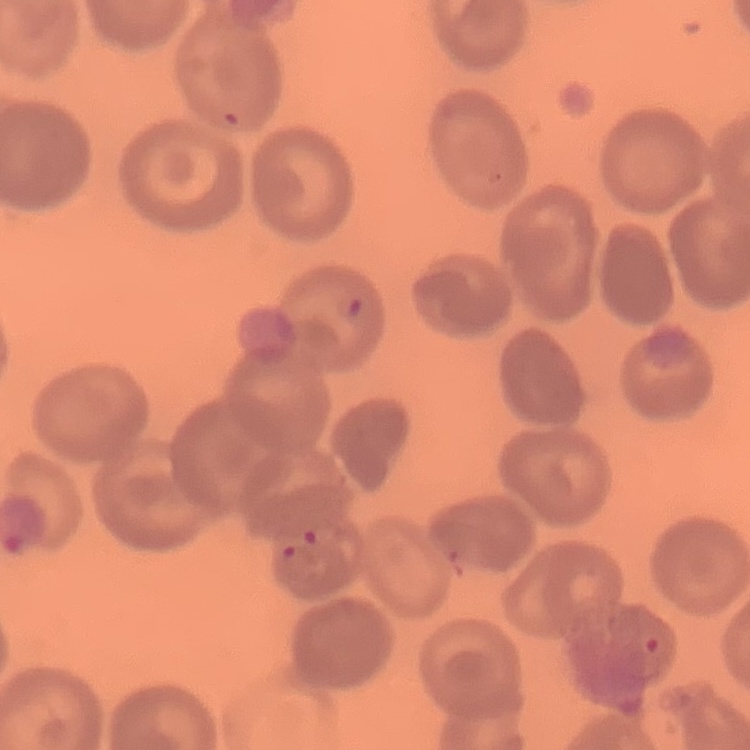 The erythrocytes show no rouleaux formation. Field's or Giemsa stain. Square crop of a larger photomicrograph. Thin blood film.